Identify the blood parasite species.
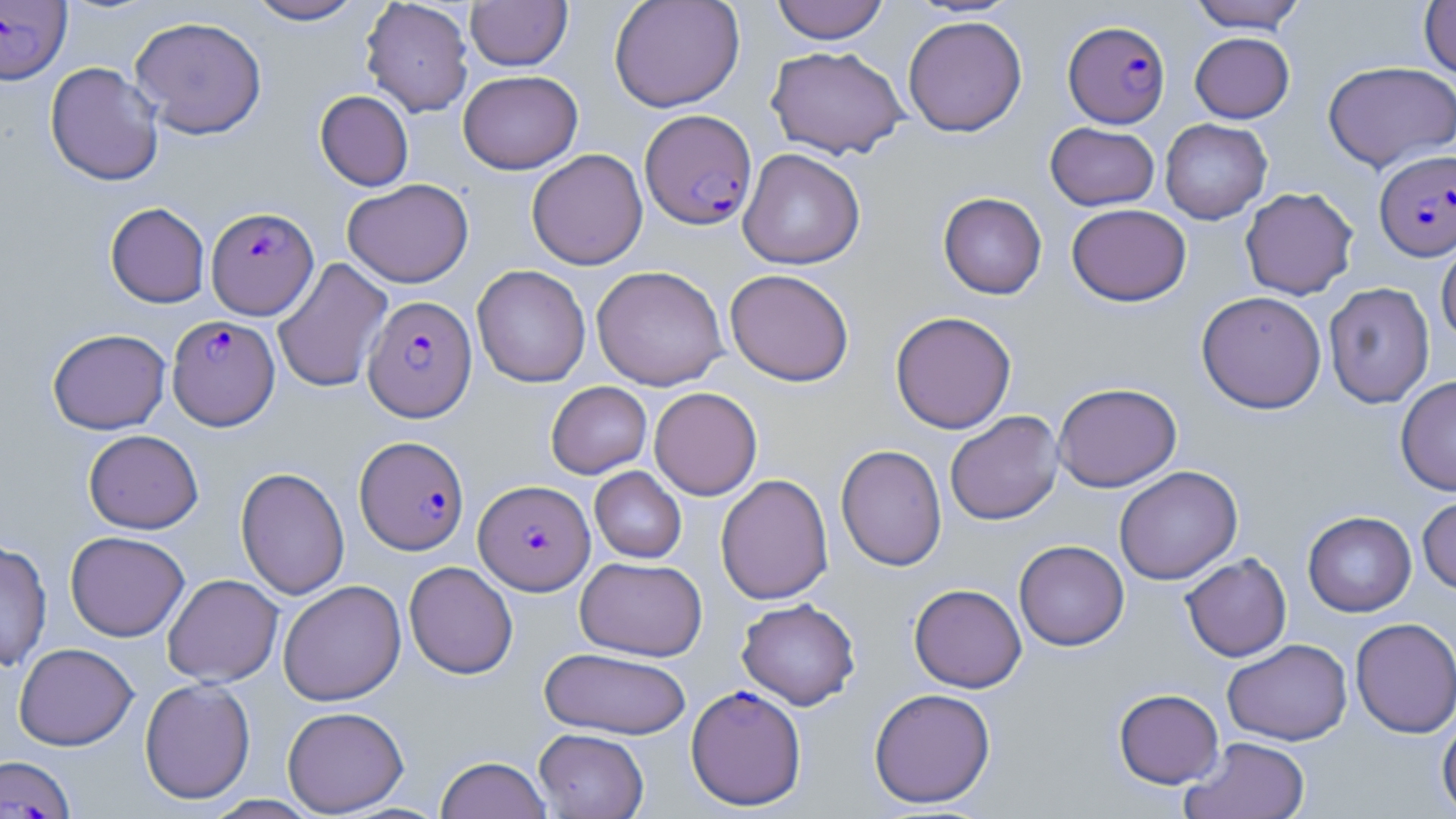

Plasmodium falciparum.

Approximate bounding boxes as [x1, y1, x2, y2] in pixels. Uninfected red blood cell locations (subset): [245, 0, 366, 25], [465, 0, 572, 70], [609, 0, 745, 112], [770, 0, 890, 44], [1187, 0, 1308, 33], [360, 1, 474, 117], [1419, 1, 1456, 80], [129, 15, 267, 139], [902, 15, 1028, 136], [1189, 32, 1294, 123], [766, 45, 909, 159], [1322, 60, 1456, 171], [45, 61, 164, 186], [457, 70, 582, 174], [315, 90, 413, 191], [1160, 118, 1272, 224], [1045, 122, 1159, 210], [738, 148, 865, 269], [526, 149, 648, 270], [342, 178, 474, 287], [1240, 187, 1358, 300], [938, 192, 1047, 299], [105, 202, 210, 308], [1067, 203, 1191, 306], [1436, 234, 1456, 347], [272, 258, 393, 393], [591, 264, 729, 390], [472, 265, 591, 387], [724, 269, 855, 387], [1323, 282, 1434, 408], [1196, 291, 1327, 414], [890, 311, 1017, 434], [47, 328, 171, 434], [1395, 375, 1456, 496], [546, 381, 652, 479], [1053, 382, 1182, 492], [649, 387, 762, 500], [944, 410, 1064, 525], [83, 429, 203, 533], [835, 444, 948, 572], [1114, 465, 1243, 585], [235, 466, 350, 600], [590, 466, 686, 563], [715, 473, 834, 605], [1417, 493, 1456, 594], [1303, 511, 1417, 617], [65, 530, 189, 642], [1014, 540, 1129, 650], [0, 541, 52, 671], [1180, 553, 1292, 661], [575, 556, 706, 661], [404, 561, 518, 679], [162, 574, 283, 687], [278, 580, 406, 706], [909, 583, 1027, 693], [736, 598, 860, 710], [1350, 617, 1456, 738], [1222, 639, 1353, 745], [14, 643, 138, 750], [539, 646, 692, 739], [139, 677, 255, 804], [868, 687, 996, 808], [1113, 688, 1224, 788], [283, 706, 409, 816], [1436, 714, 1456, 818], [534, 728, 649, 818], [1181, 736, 1311, 819], [435, 756, 552, 819]. Plasmodium falciparum-infected red blood cell locations (subset): [0, 1, 71, 84], [1063, 20, 1171, 128], [639, 109, 757, 230], [1375, 150, 1456, 261], [206, 206, 319, 320], [362, 295, 476, 421], [167, 314, 280, 430], [355, 435, 469, 555], [474, 479, 594, 595], [686, 684, 807, 810]. Image is 1456×819 pixels. Captured at 1000x magnification. May-Grünwald-Giemsa-stained preparation. Thin blood smear. Optical microscopy. Single field of view.